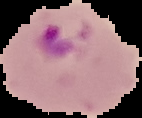 Image is 142×118 pixels. From a thin blood film. Result: malaria parasites identified. The area outside the segmented cell region is set to black.